Classify this cell by malaria status.
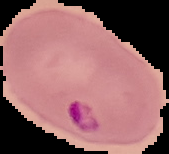

It is parasitized.

Summary:
  - Image type: cell region segmented out of the field of view; surrounding area masked to black
  - Image size: 169×154 pixels
  - Preparation: thin blood film